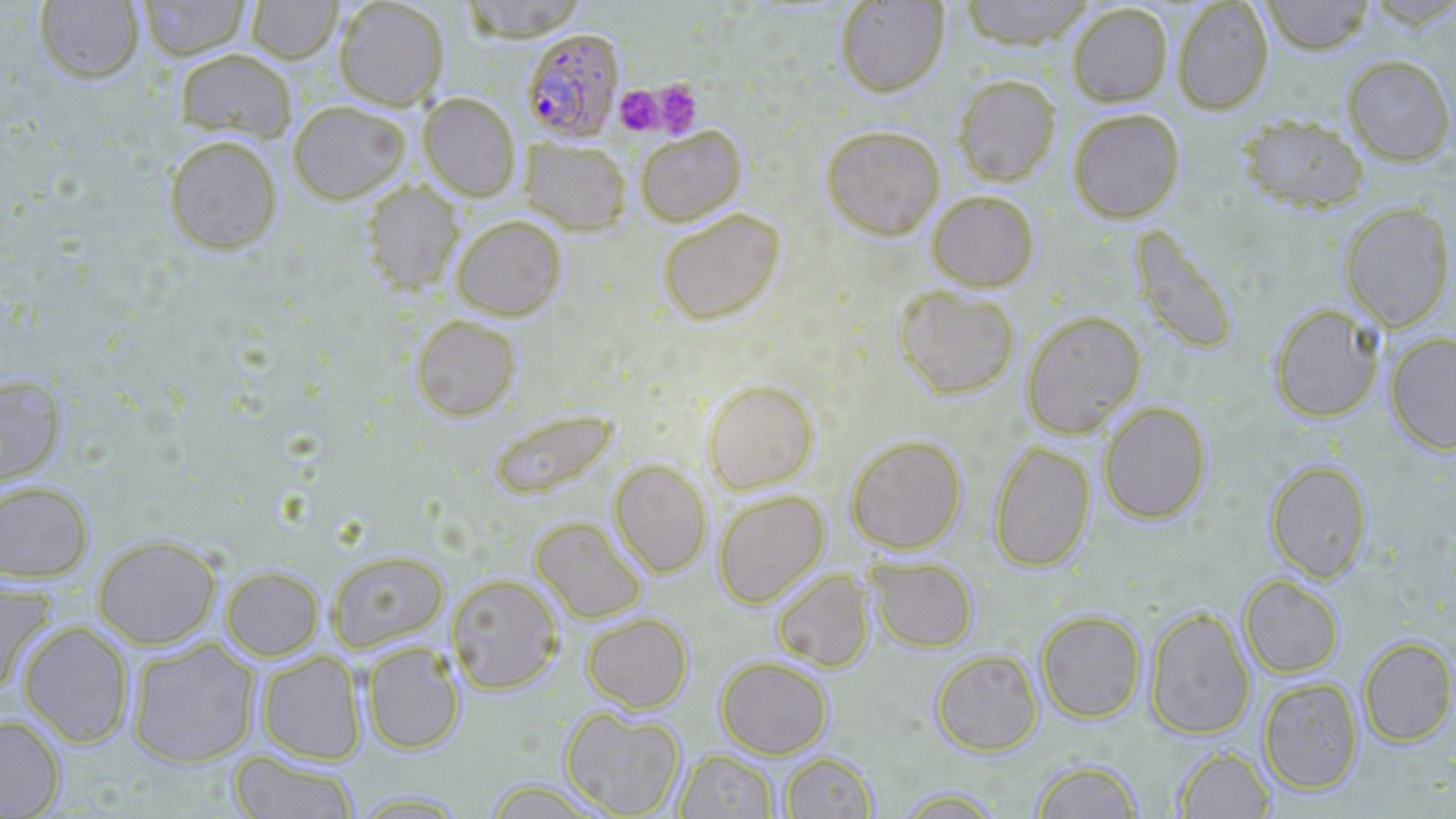 Approximate bounding boxes as named x1/y1/x2/y2 corners in pixels. Platelet locations: (x1=649, y1=79, x2=702, y2=137), (x1=614, y1=84, x2=667, y2=135). Plasmodium falciparum-infected red blood cell locations: (x1=521, y1=28, x2=625, y2=143). Uninfected red blood cell locations: (x1=34, y1=0, x2=145, y2=83), (x1=136, y1=0, x2=252, y2=60), (x1=245, y1=0, x2=343, y2=63), (x1=333, y1=0, x2=449, y2=110), (x1=458, y1=0, x2=588, y2=41), (x1=957, y1=0, x2=1097, y2=48), (x1=1172, y1=0, x2=1273, y2=114), (x1=1260, y1=0, x2=1375, y2=54), (x1=835, y1=1, x2=949, y2=96), (x1=1067, y1=2, x2=1173, y2=107), (x1=174, y1=48, x2=297, y2=142), (x1=1341, y1=54, x2=1456, y2=166), (x1=952, y1=74, x2=1061, y2=186), (x1=418, y1=92, x2=520, y2=200), (x1=288, y1=100, x2=410, y2=204), (x1=1067, y1=107, x2=1186, y2=223), (x1=1236, y1=112, x2=1369, y2=212), (x1=820, y1=125, x2=945, y2=239), (x1=635, y1=126, x2=745, y2=226), (x1=163, y1=135, x2=283, y2=254), (x1=520, y1=138, x2=631, y2=235), (x1=360, y1=180, x2=465, y2=294), (x1=926, y1=189, x2=1040, y2=291), (x1=1339, y1=201, x2=1455, y2=333), (x1=657, y1=208, x2=785, y2=325), (x1=451, y1=214, x2=567, y2=321), (x1=1128, y1=225, x2=1240, y2=355), (x1=894, y1=285, x2=1021, y2=399), (x1=1268, y1=303, x2=1385, y2=423), (x1=1021, y1=310, x2=1146, y2=437), (x1=411, y1=314, x2=522, y2=421), (x1=1385, y1=331, x2=1456, y2=455), (x1=0, y1=374, x2=66, y2=486), (x1=701, y1=378, x2=819, y2=493), (x1=1098, y1=401, x2=1213, y2=524), (x1=488, y1=408, x2=619, y2=500), (x1=845, y1=434, x2=967, y2=555), (x1=988, y1=440, x2=1095, y2=572), (x1=609, y1=460, x2=712, y2=578), (x1=1264, y1=460, x2=1373, y2=582), (x1=0, y1=479, x2=95, y2=583), (x1=712, y1=490, x2=829, y2=608), (x1=529, y1=516, x2=648, y2=624), (x1=92, y1=534, x2=222, y2=649), (x1=327, y1=550, x2=449, y2=651), (x1=865, y1=555, x2=979, y2=652), (x1=221, y1=565, x2=324, y2=660), (x1=771, y1=568, x2=876, y2=672), (x1=446, y1=573, x2=563, y2=694), (x1=1239, y1=575, x2=1344, y2=678), (x1=0, y1=577, x2=57, y2=693), (x1=1145, y1=606, x2=1255, y2=739), (x1=1036, y1=609, x2=1146, y2=723), (x1=581, y1=612, x2=693, y2=713), (x1=17, y1=620, x2=134, y2=747), (x1=1357, y1=636, x2=1456, y2=746), (x1=126, y1=638, x2=260, y2=767), (x1=361, y1=641, x2=466, y2=755), (x1=931, y1=649, x2=1043, y2=756), (x1=256, y1=650, x2=367, y2=765), (x1=715, y1=655, x2=833, y2=759), (x1=1258, y1=677, x2=1363, y2=795), (x1=560, y1=705, x2=686, y2=818), (x1=0, y1=714, x2=66, y2=818), (x1=1173, y1=745, x2=1276, y2=818), (x1=674, y1=749, x2=779, y2=819), (x1=229, y1=750, x2=360, y2=819), (x1=779, y1=751, x2=878, y2=818), (x1=1030, y1=759, x2=1144, y2=818), (x1=481, y1=779, x2=611, y2=818), (x1=892, y1=788, x2=1006, y2=817), (x1=346, y1=790, x2=473, y2=817). Slide-level diagnosis: Plasmodium falciparum. Optical microscopy. May-Grünwald-Giemsa-stained preparation. Single field of view. Thin blood smear. Image is 1456×819 pixels. 1000x magnification.